Report the malaria status.
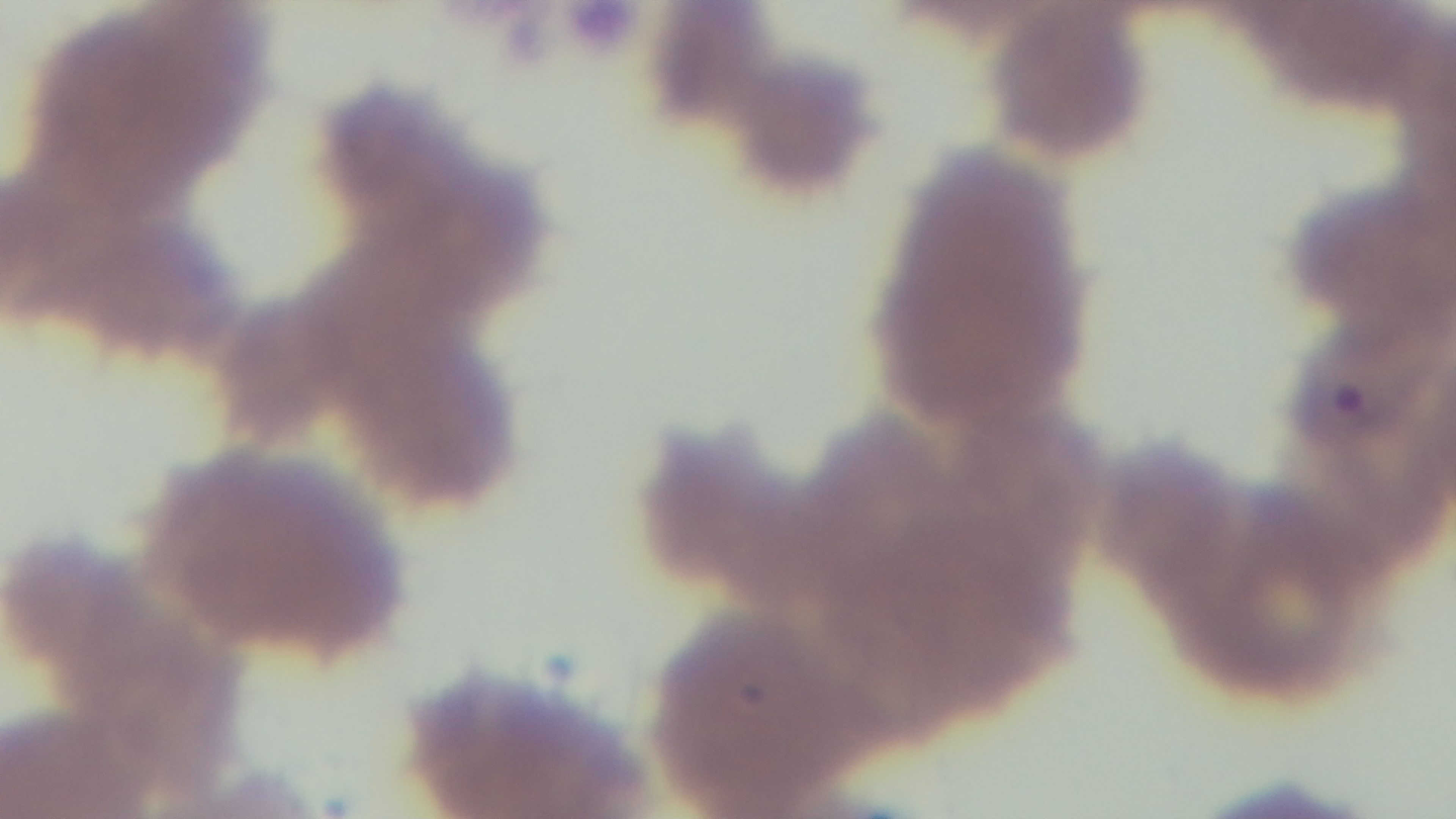

It is infected.

preparation: thin smear
field_of_view: single
objective: 100x oil immersion
modality: light microscopy
stain: Giemsa
capture: mounted 4K digital camera